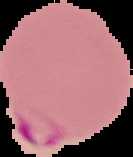

Cell region segmented out of the field of view; the surrounding area is masked to black. Result: Plasmodium parasites detected. Image is 133×157 pixels. From a thin blood smear.